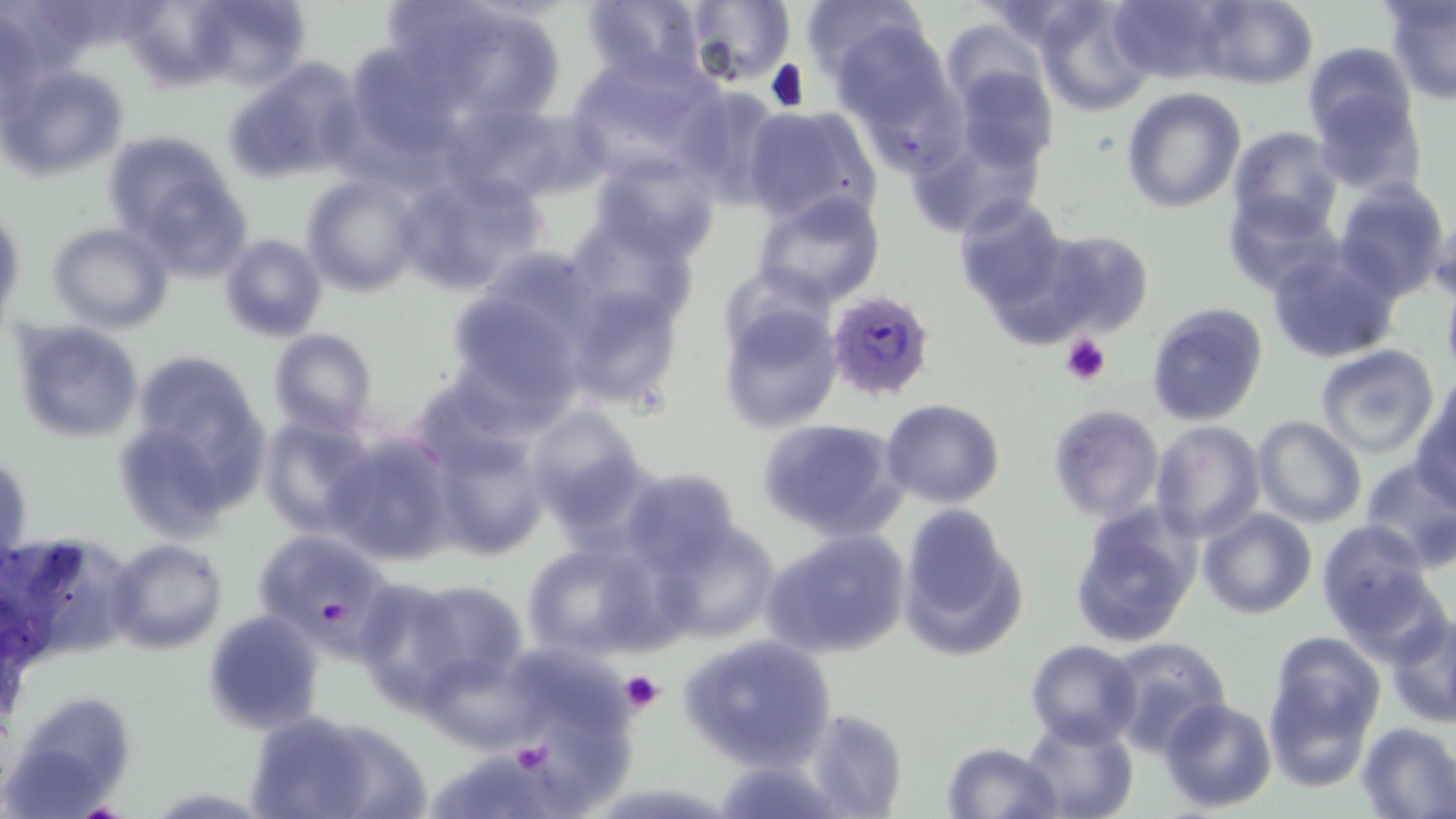
slide-level diagnosis = Plasmodium falciparum
stain = May-Grünwald-Giemsa
preparation = thin blood film
uninfected red blood cell locations = approximate bounding boxes as (x1, y1, x2, y2) in pixels: (183, 0, 316, 92), (379, 0, 567, 133), (580, 0, 708, 84), (685, 0, 794, 88), (970, 0, 1102, 47), (1107, 0, 1235, 86), (1194, 0, 1318, 90), (1033, 1, 1154, 115), (800, 2, 924, 82), (1386, 2, 1456, 105), (941, 19, 1045, 111), (831, 22, 962, 152), (340, 40, 464, 159), (1303, 41, 1415, 142), (565, 51, 729, 182), (224, 58, 365, 183), (1, 66, 129, 180), (948, 67, 1060, 176), (671, 84, 787, 207), (1122, 86, 1248, 212), (1313, 91, 1426, 197), (439, 100, 585, 206), (742, 104, 879, 227), (1228, 127, 1342, 236), (103, 133, 247, 266), (585, 152, 725, 264), (396, 166, 549, 293), (299, 172, 425, 297), (1332, 178, 1450, 301), (753, 190, 887, 308), (1225, 191, 1342, 297), (951, 193, 1071, 314), (0, 205, 24, 330), (562, 211, 700, 332), (47, 222, 173, 333), (1021, 228, 1157, 344), (219, 233, 329, 343), (1266, 247, 1401, 364), (442, 281, 589, 412), (563, 284, 687, 413), (1146, 302, 1268, 426), (719, 303, 843, 433), (10, 319, 145, 444), (267, 328, 378, 438), (1315, 344, 1438, 458), (117, 353, 272, 538), (1412, 392, 1456, 508), (880, 399, 1004, 508), (1046, 404, 1164, 522), (524, 405, 654, 537), (258, 414, 380, 539), (756, 417, 907, 542), (1252, 417, 1365, 528), (1150, 421, 1265, 542), (426, 428, 551, 562), (321, 431, 455, 567), (1, 448, 31, 569), (1357, 459, 1456, 571), (617, 468, 747, 580), (1067, 504, 1201, 648), (898, 507, 1025, 662), (1199, 508, 1316, 620), (651, 520, 783, 642), (1315, 521, 1436, 638), (251, 528, 399, 654), (762, 529, 911, 660), (0, 530, 131, 670), (107, 538, 227, 654), (521, 539, 666, 662), (347, 574, 492, 709), (401, 578, 526, 687), (202, 610, 325, 734), (1384, 613, 1456, 727), (1268, 632, 1385, 749), (676, 633, 837, 772), (1103, 635, 1231, 754), (1025, 638, 1142, 749), (421, 646, 544, 753), (521, 653, 645, 755), (1263, 673, 1373, 788), (7, 690, 136, 810), (1160, 697, 1277, 814), (801, 707, 907, 819), (245, 710, 422, 818), (1019, 714, 1139, 819), (534, 716, 643, 807), (1356, 722, 1456, 819), (942, 741, 1064, 819), (456, 744, 571, 818)
field of view = one of a larger specimen
image size = 1456×819 pixels
modality = light microscopy
platelet locations = approximate bounding boxes as (x1, y1, x2, y2) in pixels: (1060, 333, 1112, 386), (620, 670, 665, 715), (513, 744, 558, 775)
magnification = 1000x
Plasmodium falciparum-infected red blood cell locations = approximate bounding boxes as (x1, y1, x2, y2) in pixels: (829, 296, 936, 409)